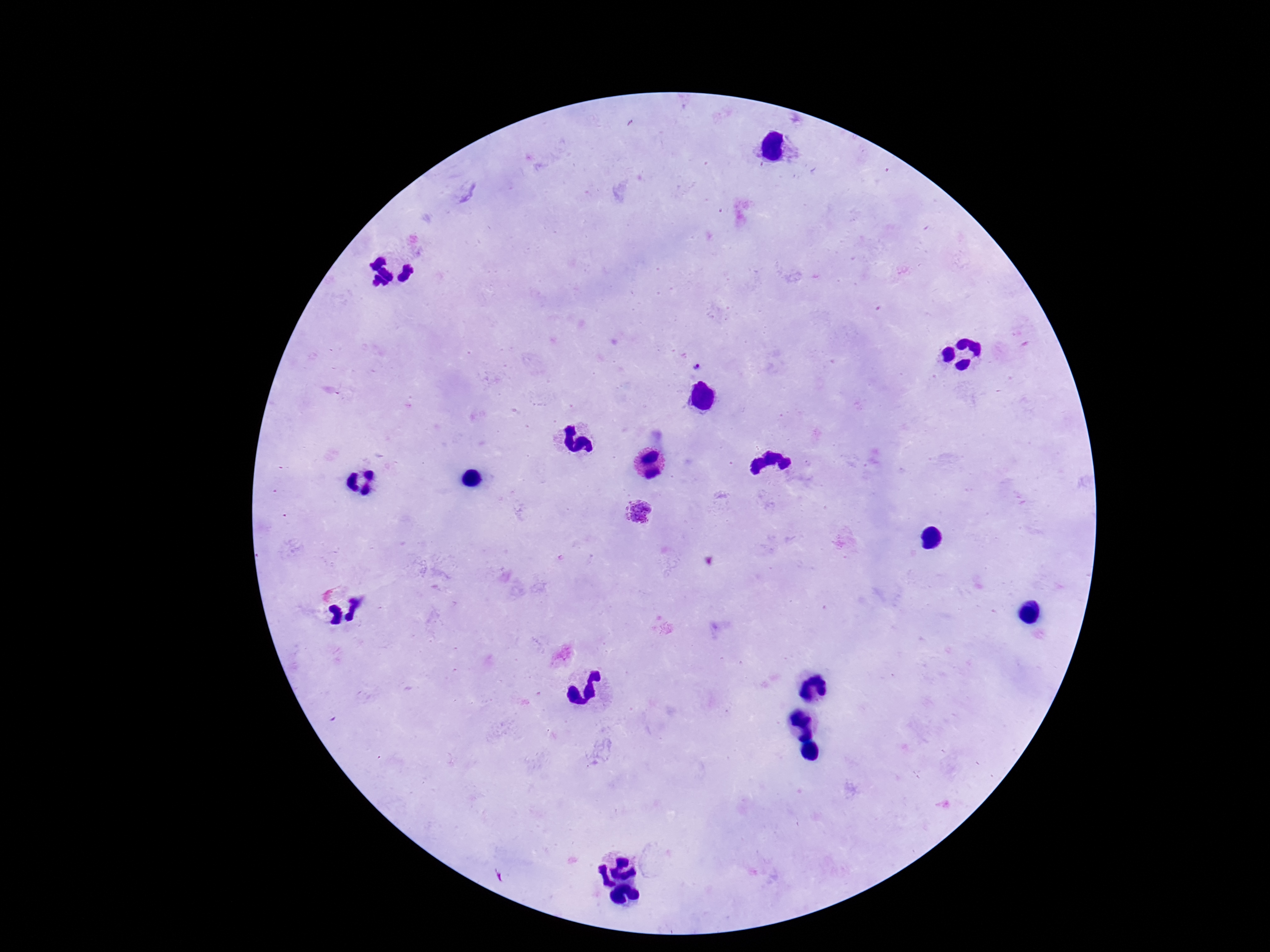

Approximate centers as (x, y) in pixels. Plasmodium parasite locations: (697, 364), (639, 513). Image is 1270×952 pixels. Photographed through the microscope eyepiece with a smartphone camera. Patient malaria status: positive. Thick blood film. Single field of view. Giemsa stain. 100x magnification.